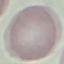
Summary:
  - Result: negative for malaria parasites
  - Stain: Giemsa
  - Preparation: thin blood smear
  - Image type: automatically extracted cell patch, resized to 64 × 64 pixels
  - Capture: smartphone through the microscope eyepiece